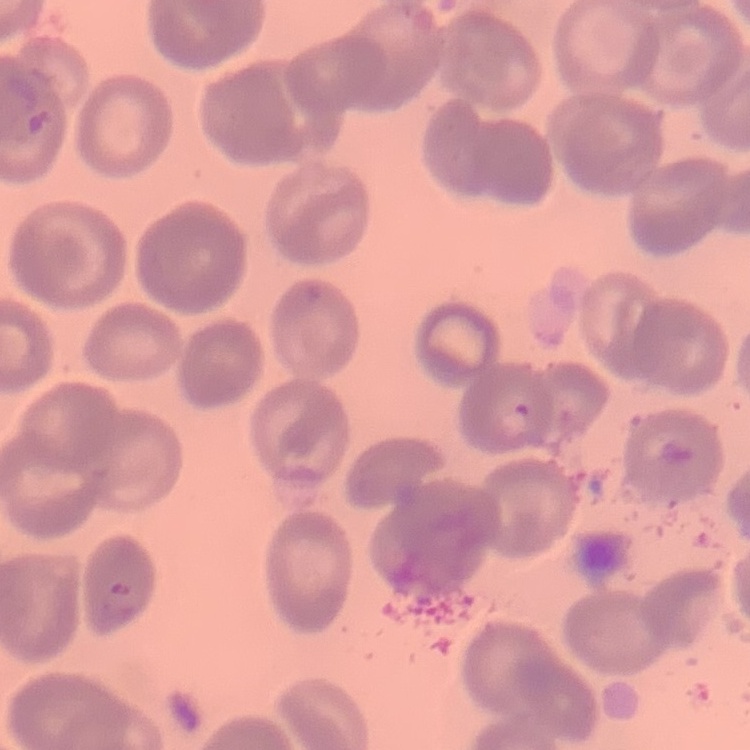

The red blood cells exhibit no rouleaux formation. One tile cut from a larger photomicrograph. Thin blood smear. Stained with either Field's or Giemsa.